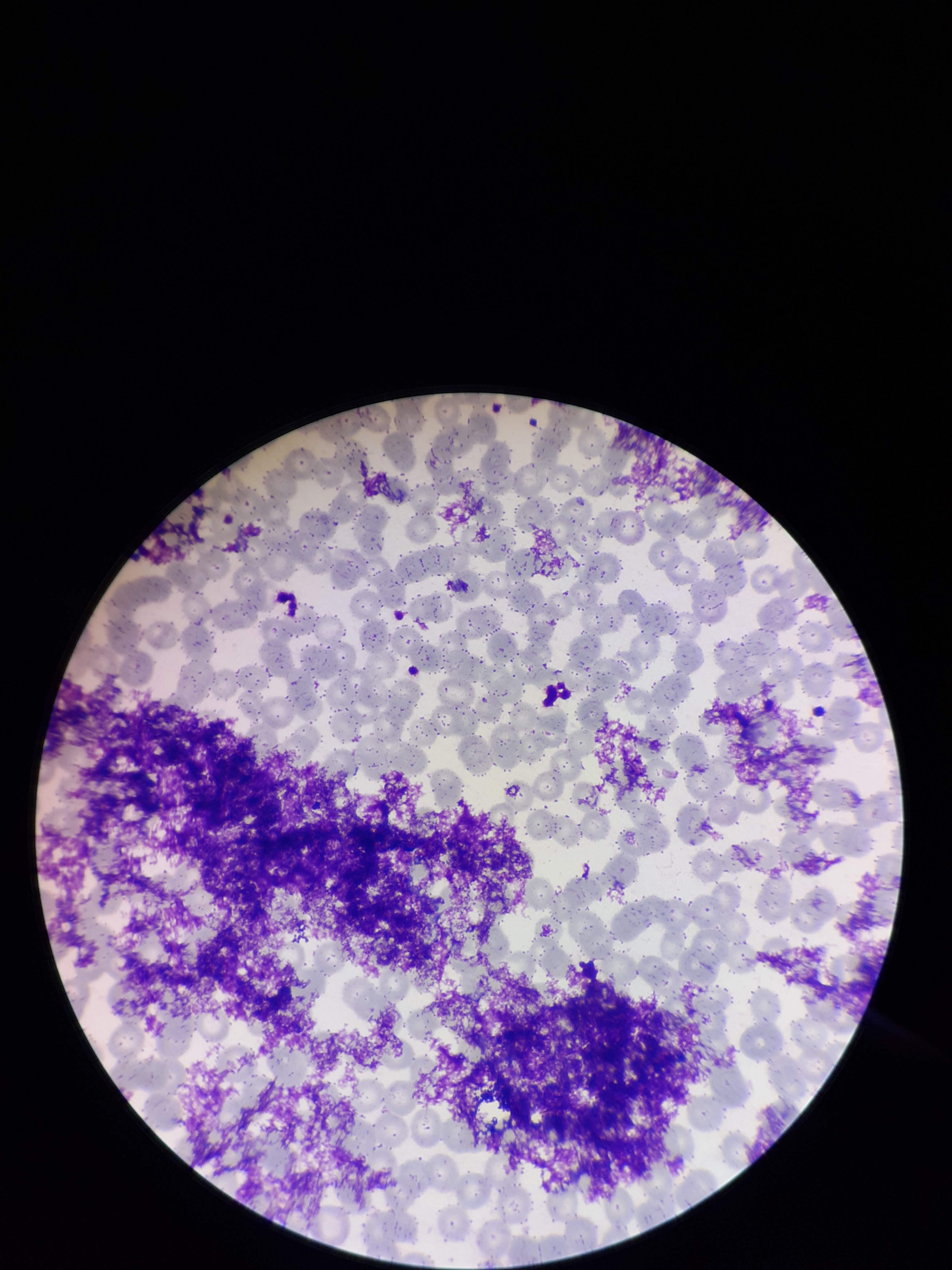
Summary:
  - Preparation: thin smear
  - Red blood cell count: 290
  - Image size: 952×1270 pixels
  - Parasitized red blood cells: none detected
  - Parasitized red blood cell count: 0
  - Patient malaria status: negative
  - Stain: Giemsa
  - Field of view: single
  - Capture: smartphone photograph through the microscope eyepiece